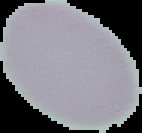
Segmented cell region on a black background. Image is 142×133 pixels. Malaria status: uninfected. From a thin blood smear.